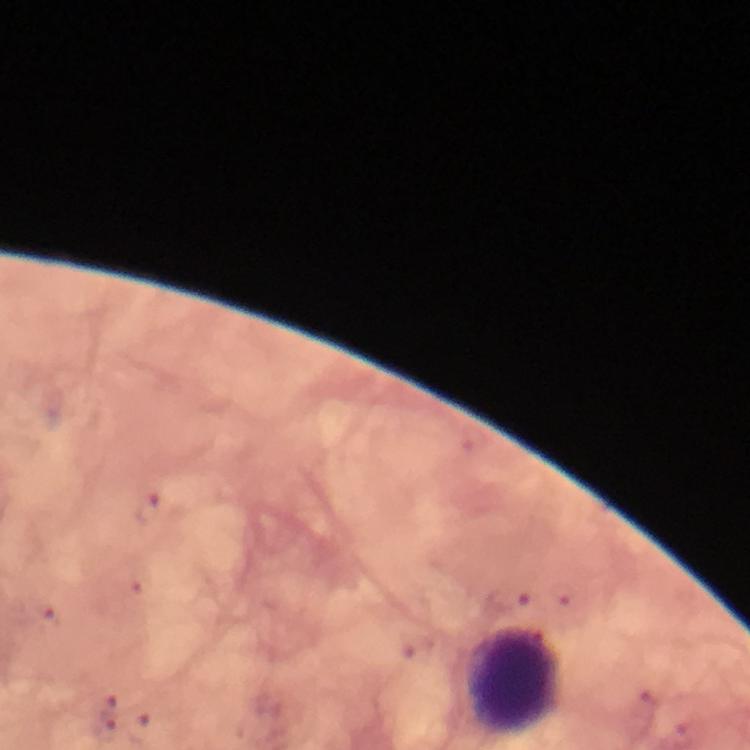

Approximate centers as {x, y} in pixels.
Summary:
  - Leukocyte locations: {515, 680}
  - Immersion oil: applied
  - Magnification: 100x
  - Context: from a diagnostic examination for malaria
  - Cropped from: one field of view
  - Capture: smartphone mounted on the microscope
  - Stain: Giemsa
  - Plasmodium parasites: none seen
  - Image size: 750×750 pixels
  - Preparation: thick blood smear